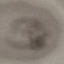 Malaria status: parasitized. Giemsa stain. Thin smear of blood. Acquired by smartphone through the microscope eyepiece. Automatically extracted cell patch, resized to 64 × 64 pixels.